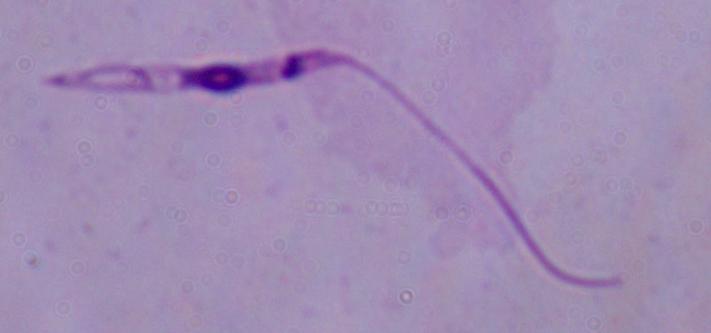
Captured at 1000x magnification. Micrograph. A Leishmania parasite is seen.